Comment on the morphology of the red blood cells.
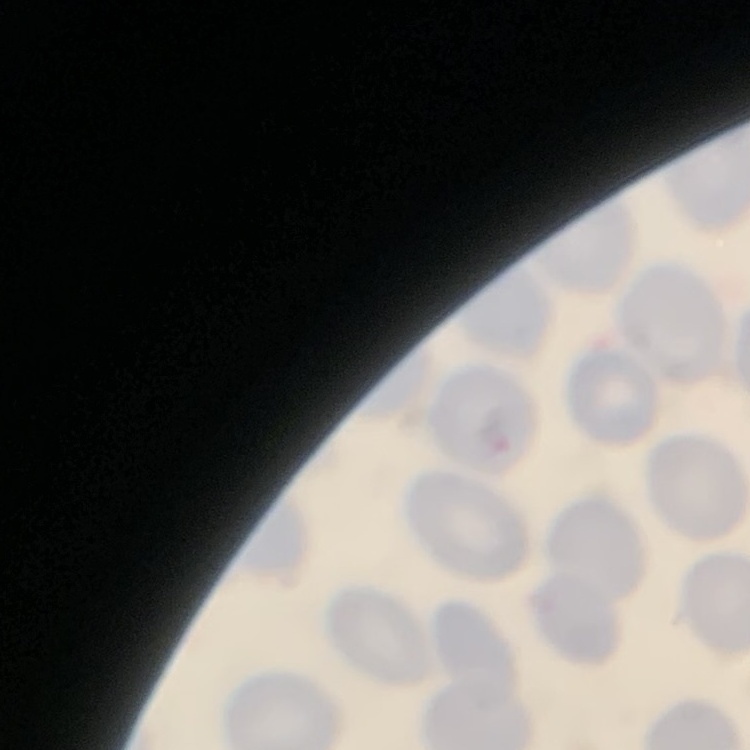
They show no rouleaux formation.

Summary:
  - Stain: Field's or Giemsa
  - Image type: square crop of a larger photomicrograph
  - Preparation: thin peripheral smear